Comment on the morphology of the red blood cells.
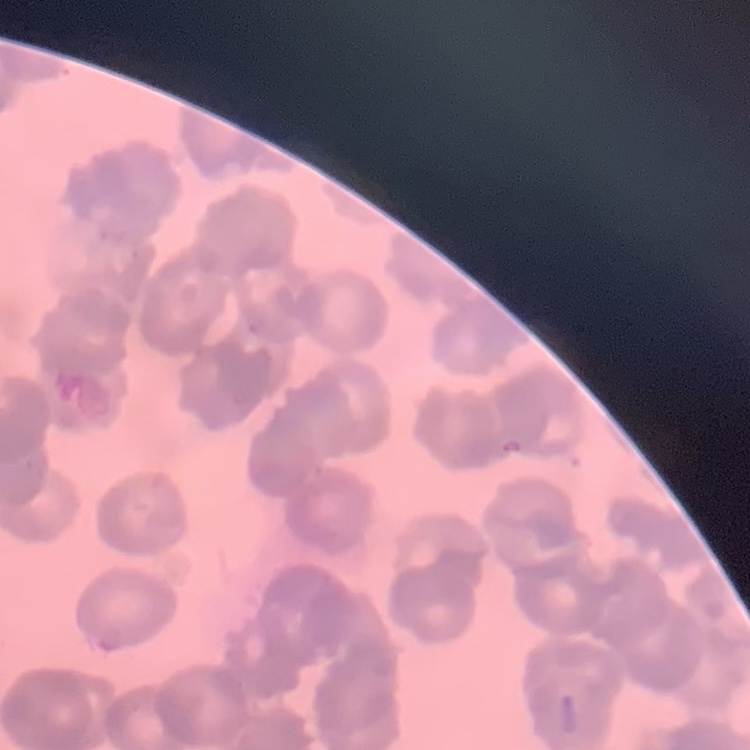
They show rouleaux formation.

Field's or Giemsa stain. Thin peripheral smear. One tile cut from a larger photomicrograph.